State the blood parasite species.
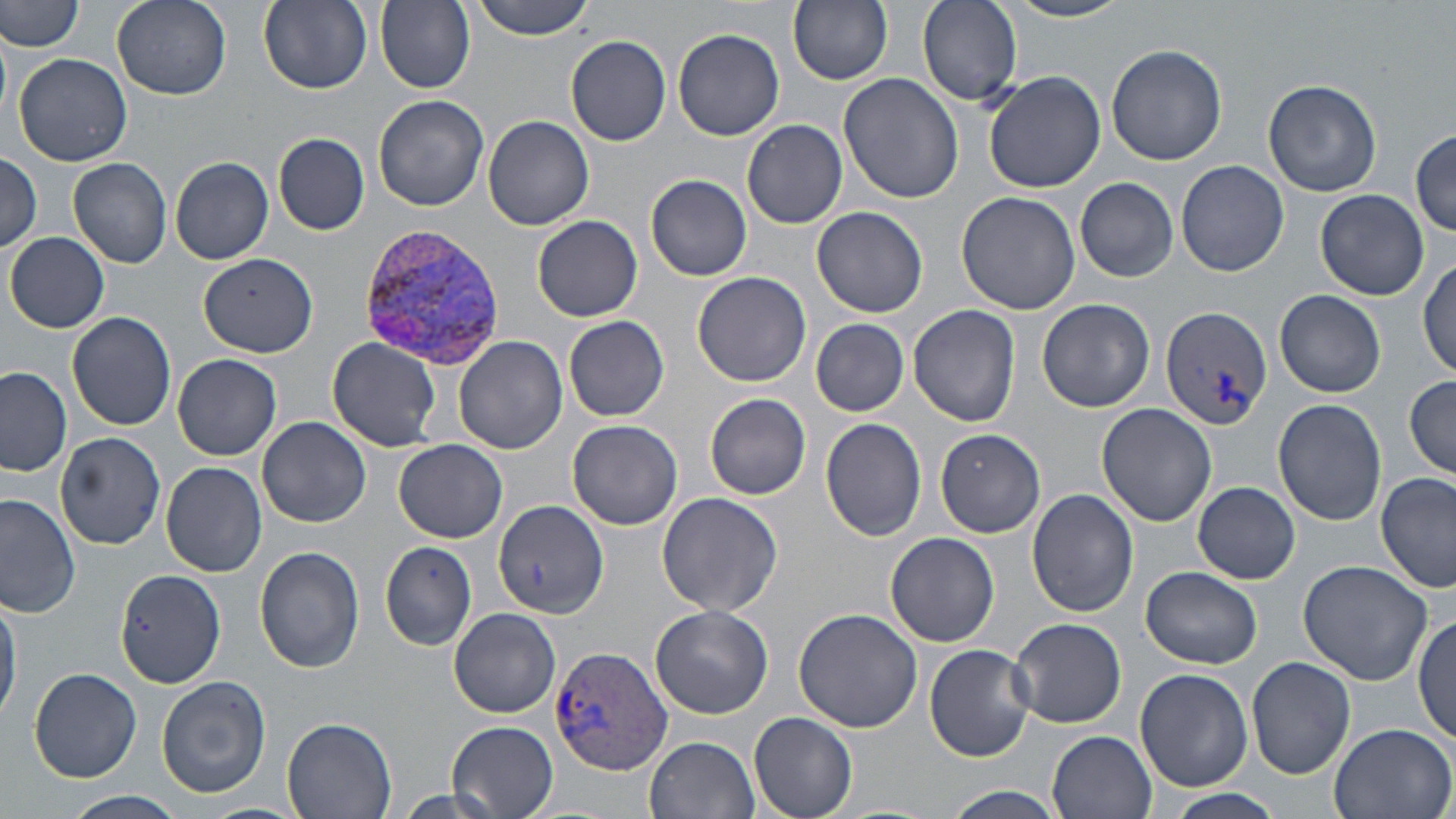
Plasmodium vivax.

Summary:
  - Coordinate format: approximate bounding boxes as (x1, y1, x2, y2) in pixels
  - Plasmodium vivax-infected red blood cell locations: (354, 225, 503, 364), (1159, 305, 1272, 430), (548, 647, 672, 772)
  - Uninfected red blood cell locations: (1, 0, 84, 52), (112, 0, 231, 99), (259, 0, 373, 92), (376, 0, 475, 91), (470, 0, 597, 39), (788, 0, 894, 86), (918, 0, 1022, 105), (1005, 0, 1135, 24), (673, 28, 785, 140), (566, 36, 672, 146), (1105, 44, 1229, 167), (12, 53, 134, 169), (984, 70, 1107, 193), (838, 75, 965, 206), (1262, 80, 1382, 197), (373, 95, 489, 212), (483, 115, 595, 231), (742, 120, 847, 228), (1411, 128, 1456, 235), (273, 133, 370, 235), (0, 152, 43, 253), (170, 156, 273, 264), (68, 157, 172, 269), (1175, 160, 1288, 277), (646, 173, 752, 280), (1076, 179, 1179, 283), (1316, 189, 1428, 300), (955, 191, 1082, 316), (810, 206, 928, 318), (532, 215, 643, 321), (5, 232, 110, 333), (198, 255, 322, 357), (1417, 257, 1455, 380), (692, 270, 812, 387), (1276, 289, 1386, 398), (1037, 298, 1155, 413), (908, 305, 1022, 428), (67, 312, 177, 432), (563, 315, 670, 422), (810, 318, 910, 416), (327, 337, 443, 452), (454, 337, 567, 455), (172, 353, 282, 460), (1, 367, 72, 477), (1403, 376, 1456, 478), (704, 392, 811, 499), (1273, 399, 1387, 526), (1097, 404, 1217, 527), (258, 415, 371, 527), (819, 417, 927, 542), (566, 419, 683, 530), (933, 428, 1045, 538), (55, 431, 166, 550), (393, 440, 507, 541), (160, 461, 266, 577), (1376, 470, 1455, 594), (1194, 480, 1302, 584), (1027, 489, 1138, 617), (656, 492, 783, 617), (0, 495, 78, 618), (493, 501, 609, 619), (884, 532, 999, 646), (378, 542, 477, 649), (255, 546, 365, 673), (1297, 559, 1433, 685), (1140, 565, 1263, 668), (116, 568, 225, 688), (1, 591, 21, 722), (650, 605, 773, 718), (448, 606, 559, 718), (793, 608, 922, 733), (1414, 613, 1454, 745), (1008, 617, 1127, 729), (925, 642, 1037, 762), (1246, 656, 1355, 779), (29, 667, 142, 781), (1135, 668, 1252, 791), (157, 675, 271, 799), (750, 712, 858, 819), (281, 715, 397, 819), (446, 720, 559, 816), (1326, 721, 1456, 819), (1046, 730, 1159, 819), (645, 735, 759, 818), (386, 787, 516, 819), (937, 787, 1072, 819), (1157, 789, 1287, 819), (66, 790, 184, 819), (195, 802, 311, 819)
  - Modality: optical microscopy
  - Preparation: thin blood smear
  - Image size: 1456×819 pixels
  - Magnification: 1000x
  - Stain: May-Grünwald-Giemsa
  - Field of view: single